Classify this cell by malaria status.
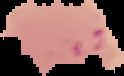
Parasitized.

image type = segmented cell region on a black background
image size = 124×76 pixels
preparation = thin blood film